Locate and identify every blood parasite.
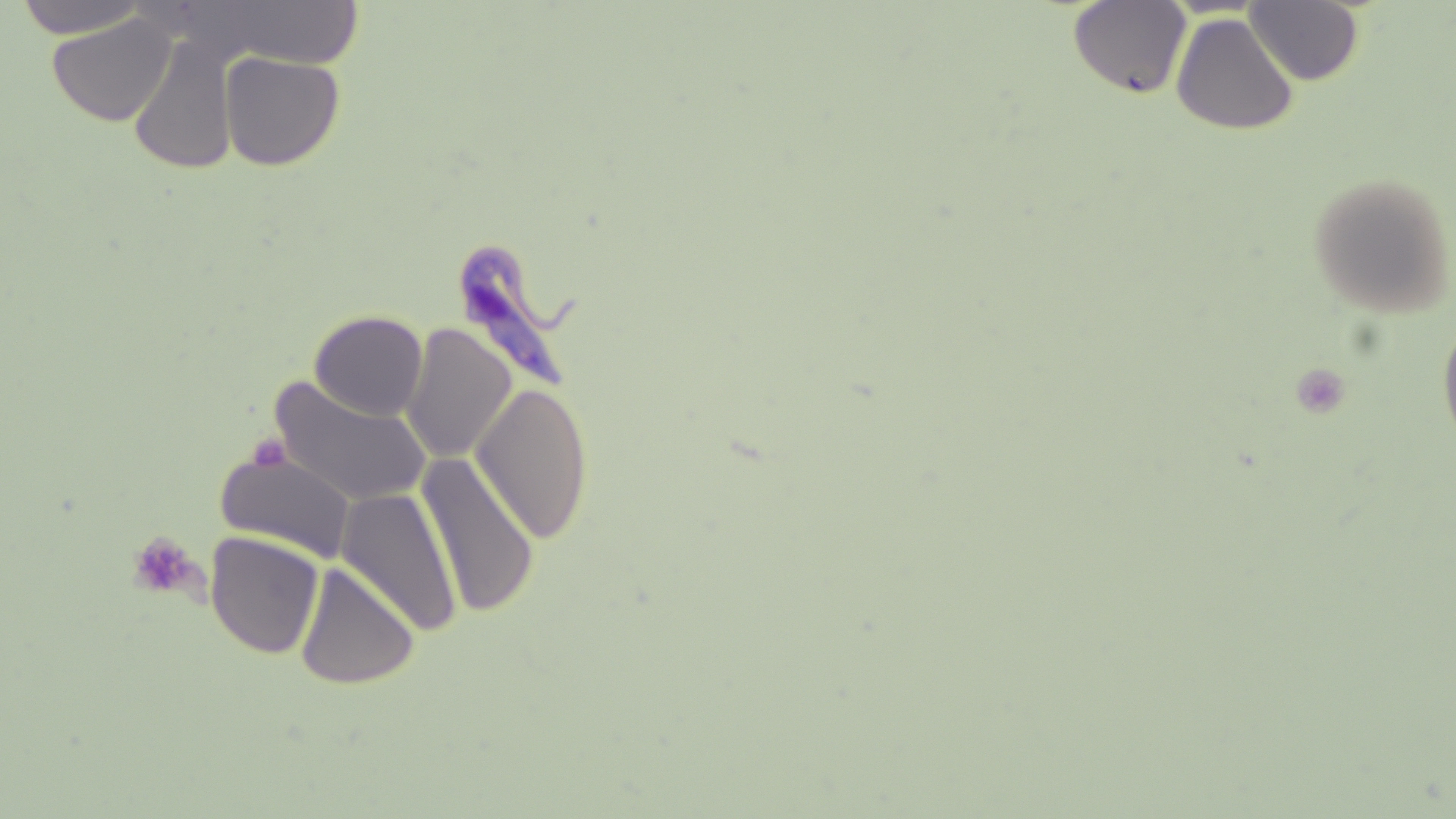
Approximate bounding boxes as named x1/y1/x2/y2 corners in pixels.
Trypanosoma brucei: (x1=453, y1=242, x2=584, y2=390).
No Plasmodium falciparum, Plasmodium ovale, Plasmodium malariae, Plasmodium vivax, or Babesia divergens observed.

Platelet locations: (x1=248, y1=435, x2=291, y2=473), (x1=127, y1=531, x2=201, y2=599). Uninfected red blood cell locations: (x1=14, y1=0, x2=149, y2=39), (x1=204, y1=1, x2=371, y2=68), (x1=1067, y1=1, x2=1192, y2=99), (x1=1245, y1=1, x2=1365, y2=86), (x1=48, y1=13, x2=177, y2=126), (x1=1171, y1=13, x2=1299, y2=135), (x1=128, y1=33, x2=238, y2=177), (x1=219, y1=51, x2=345, y2=171), (x1=1307, y1=171, x2=1455, y2=318), (x1=309, y1=309, x2=429, y2=420), (x1=1436, y1=313, x2=1456, y2=454), (x1=401, y1=322, x2=518, y2=464), (x1=270, y1=377, x2=432, y2=507), (x1=471, y1=381, x2=595, y2=544), (x1=214, y1=449, x2=356, y2=563), (x1=417, y1=454, x2=541, y2=620), (x1=336, y1=486, x2=461, y2=637), (x1=205, y1=531, x2=325, y2=659), (x1=294, y1=562, x2=420, y2=690). Slide-level diagnosis: Trypanosoma brucei. Thin blood film. Captured at 1000x magnification. Light microscopy. May-Grünwald-Giemsa-stained preparation. Image is 1456×819 pixels. Single field of view.